Assess this cell for malaria.
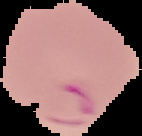
Parasitized.

image type = cell region segmented out of the field of view; surrounding area masked to black
image size = 142×136 pixels
preparation = thin blood smear